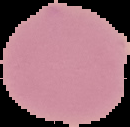
preparation = thin blood film
image type = cell region segmented out of the field of view; surrounding area masked to black
malaria status = uninfected
image size = 130×127 pixels